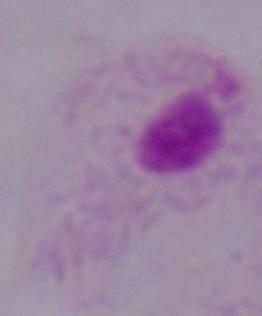
A trichomonad is shown. Micrograph. Captured at 1000x magnification.